Classify this cell by malaria status.
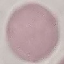
It is uninfected.

Summary:
  - Image type: automatically extracted cell patch, resized to 64 × 64 pixels
  - Capture: smartphone through the microscope eyepiece
  - Stain: Giemsa
  - Preparation: thin blood smear